Give the position of every P. falciparum parasite, noting its life-cycle stage.
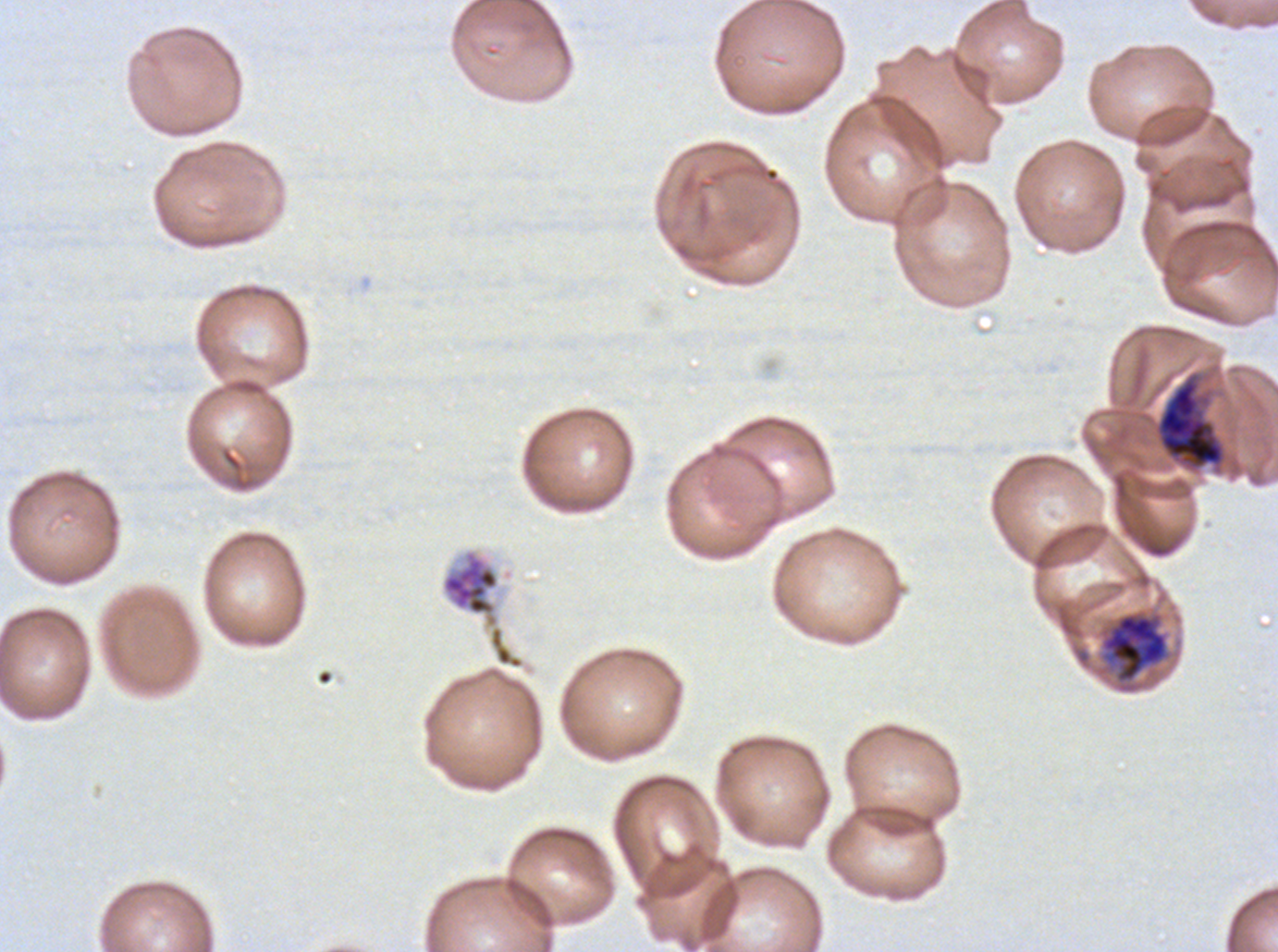

Approximate bounding boxes as {x1, y1, x2, y2} in pixels.
Late trophozoites: {1100, 611, 1169, 684}.
Late schizonts: {1154, 372, 1226, 471}.
Segmenters: {441, 549, 524, 670}.
No rings, late-ring/early-trophozoite forms, mid trophozoites, early schizonts, or gametocytes observed.

image size = 1278×952 pixels
life-cycle stages observed = late trophozoite, late schizont, segmenter
stain = Giemsa
specimen = P. falciparum cultured ex vivo for 24 to 48 hours, from a patient in The Gambia
preparation = thin blood smear
field of view = sub-image separated from a larger composite